Give the position of every leukocyte visible.
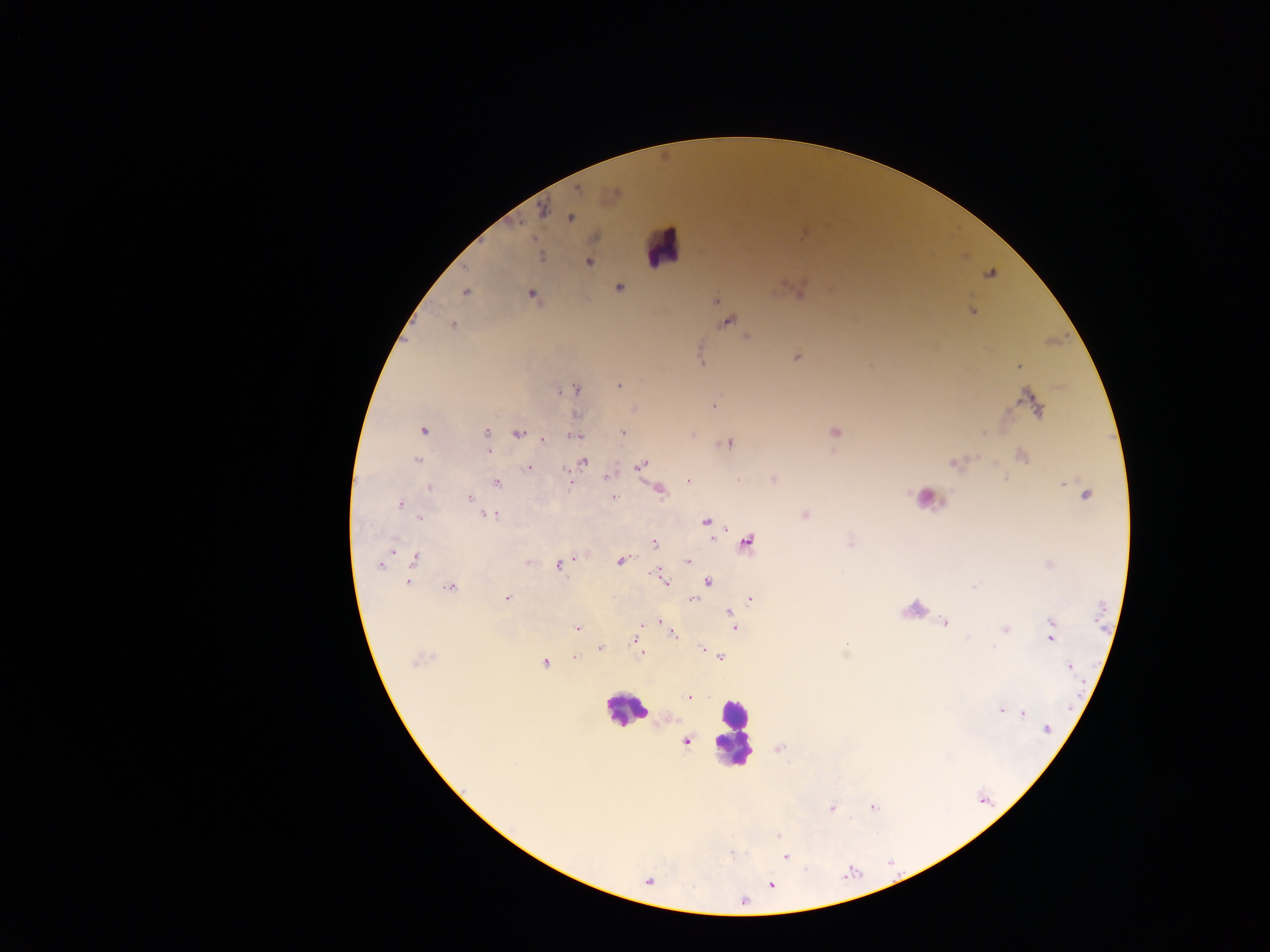

Approximate centers as [x, y] in pixels.
Leukocytes: [663, 247], [925, 501], [914, 610], [625, 709], [731, 734].

Plasmodium parasite locations: [576, 189], [541, 211], [570, 218], [540, 257], [588, 261], [990, 273], [619, 287], [798, 290], [465, 291], [532, 295], [715, 300], [970, 311], [726, 321], [452, 325], [746, 337], [797, 356], [700, 361], [1018, 365], [619, 385], [574, 389], [1031, 403], [714, 406], [634, 408], [576, 415], [423, 430], [486, 432], [622, 432], [836, 432], [519, 433], [692, 433], [575, 435], [542, 439], [728, 443], [487, 451], [1021, 455], [416, 460], [582, 461], [955, 462], [641, 464], [528, 467], [608, 476], [773, 479], [689, 480], [496, 482], [568, 482], [429, 486], [659, 490], [1085, 494], [612, 497], [470, 498], [400, 504], [480, 509], [487, 514], [805, 514], [419, 517], [705, 521], [745, 541], [850, 542], [654, 543], [389, 551], [416, 557], [621, 560], [687, 561], [527, 562], [381, 564], [1050, 564], [561, 565], [660, 574], [663, 578], [707, 581], [407, 582], [450, 587], [506, 598], [750, 598], [692, 599], [728, 612], [659, 620], [944, 622], [642, 623], [1051, 623], [734, 626], [577, 628], [1005, 628], [672, 633], [1051, 635], [636, 639], [599, 648], [702, 648], [641, 653], [574, 657], [720, 657], [420, 658], [544, 662], [1068, 666], [689, 697], [1001, 710], [1022, 713], [1046, 730], [685, 741], [779, 748], [872, 806], [831, 808], [778, 836], [731, 853], [786, 856], [647, 881], [770, 884]. Photographed through a microscope with a mobile-phone camera. One field of view. Thick blood film. Image is 1270×952 pixels. Sample from Ghana.